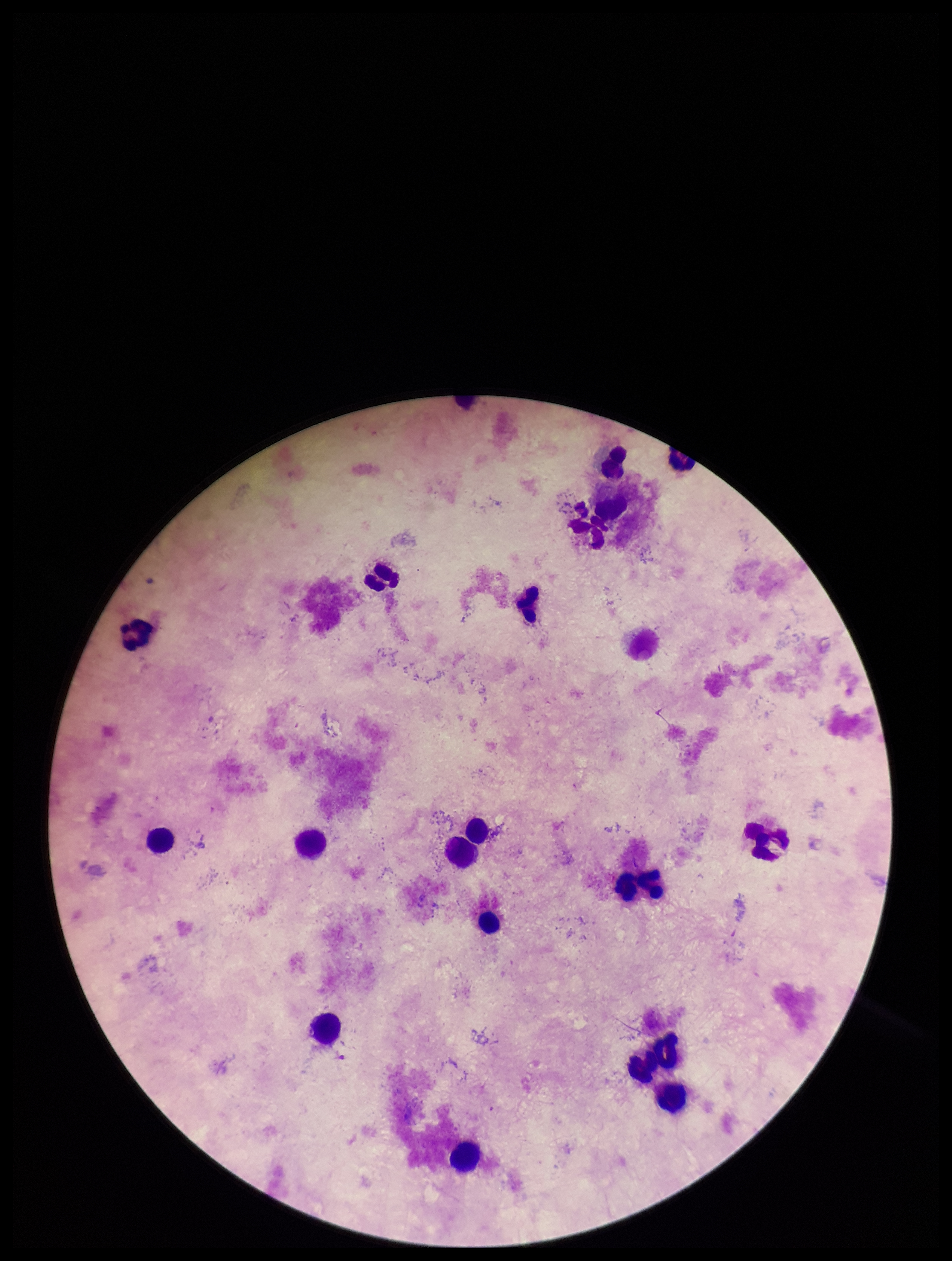

Summary:
  - Image size: 952×1261 pixels
  - Field of view: single
  - Leukocyte count: 16
  - Stain: Giemsa
  - Preparation: thick blood smear
  - Parasite count: 0
  - Capture: smartphone photograph through the microscope eyepiece
  - Plasmodium parasites: none identified
  - Patient malaria status: negative